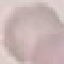 Malaria status: uninfected. Thin blood film. Giemsa-stained preparation. Acquired by smartphone through the microscope eyepiece. Cell patch, automatically extracted from a larger field of view and resized to 64 × 64 pixels.